Classify this cell by malaria status.
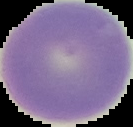

It is uninfected.

The area outside the segmented cell region is set to black. Image is 133×127 pixels. From a thin blood film.